Identify the parasite.
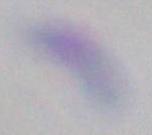
Toxoplasma gondii.

Micrograph. 1000x magnification.